Locate cells.
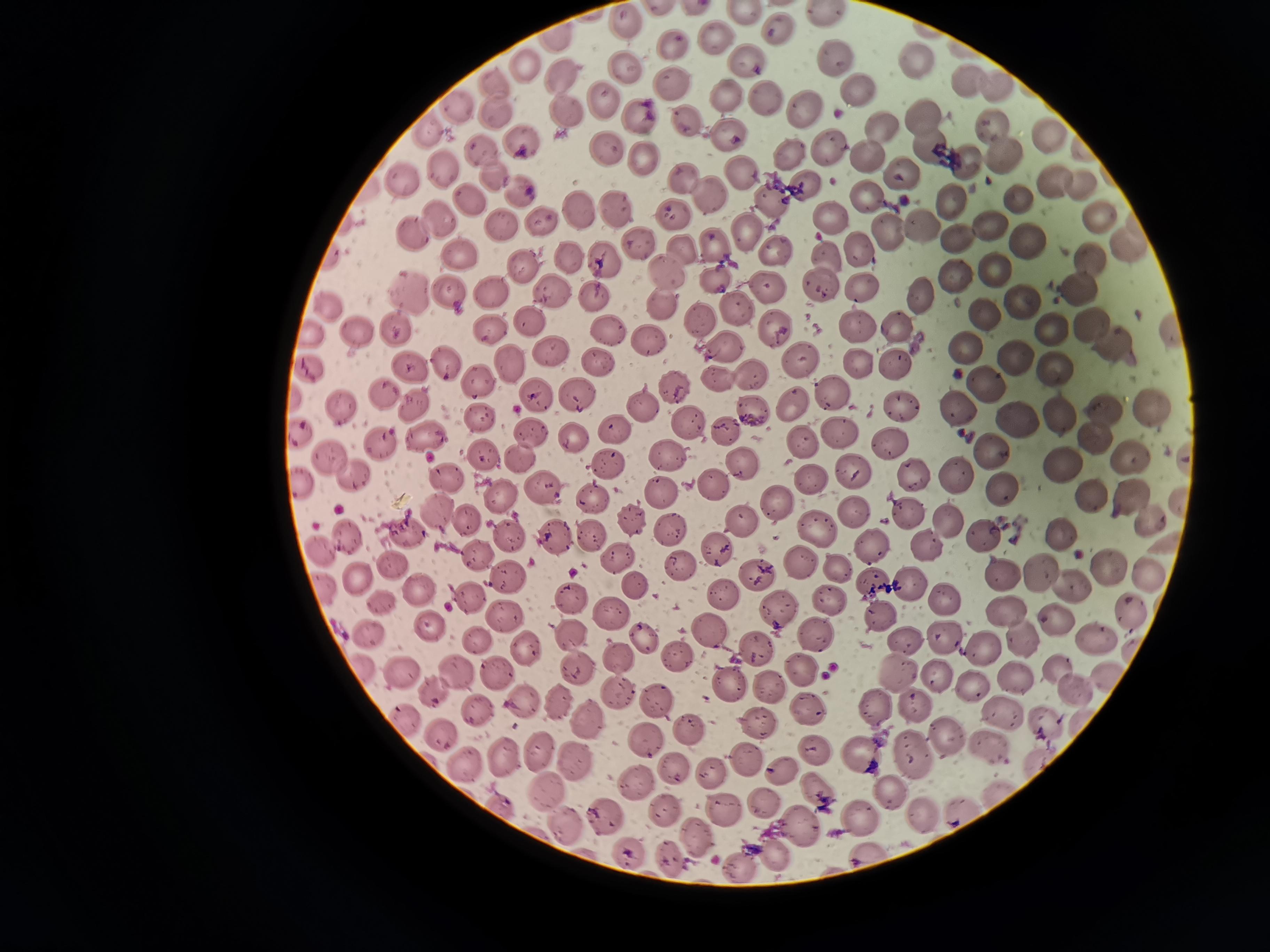

Approximate centers as [x, y] in pixels.
Cells: [625, 22], [779, 30], [715, 38], [673, 47], [835, 59], [746, 60], [910, 62], [524, 65], [625, 69], [559, 76], [964, 80], [496, 85], [671, 86], [860, 88], [996, 89], [724, 95], [603, 98], [767, 98], [803, 106], [457, 109], [498, 112], [563, 114], [636, 115], [924, 115], [993, 124], [879, 126], [728, 134], [1050, 137], [928, 141], [522, 142], [829, 146], [607, 148], [790, 150], [481, 152], [644, 155], [1004, 156], [868, 158], [967, 159], [443, 167], [739, 172], [900, 173], [683, 176], [495, 177], [403, 180], [801, 181], [1054, 182], [1080, 183], [521, 190], [709, 194], [866, 197], [470, 200], [768, 200], [1017, 201], [953, 202], [617, 209], [577, 210], [1098, 214], [673, 215], [831, 216], [541, 219], [437, 220], [504, 226], [991, 226], [918, 228], [745, 229], [956, 232], [889, 233], [412, 234], [1123, 240], [1029, 242], [639, 243], [860, 248], [683, 250], [774, 252], [459, 253], [569, 255], [604, 259], [1085, 259], [525, 265], [996, 270], [663, 272], [717, 279], [956, 281], [767, 285], [820, 285], [866, 287], [1080, 288], [408, 291], [551, 291], [922, 291], [449, 294], [594, 296], [1023, 301], [658, 303], [325, 306], [737, 308], [982, 312], [700, 316], [528, 321], [857, 326], [1095, 326], [394, 327], [1051, 328], [608, 329], [776, 329], [898, 329], [490, 330], [359, 332], [650, 340], [724, 347], [967, 348], [1113, 349], [551, 352], [1015, 354], [800, 360], [442, 361], [598, 361], [509, 363], [896, 364], [407, 365], [857, 365], [1055, 368], [717, 378], [479, 381], [987, 385], [673, 387], [834, 391], [386, 393], [533, 396], [577, 396], [414, 403], [792, 403], [903, 403], [640, 405], [956, 407], [752, 408], [1149, 410], [342, 411], [1103, 412], [1055, 416], [481, 418], [1018, 421], [687, 422], [723, 431], [836, 431], [532, 433], [426, 437], [572, 438], [891, 440], [802, 442], [1095, 442], [382, 444], [993, 451], [484, 454], [333, 456], [522, 456], [667, 456], [1126, 457], [740, 462], [607, 464], [1062, 467], [854, 470], [958, 474], [912, 475], [349, 479], [447, 479], [811, 482], [714, 483], [1000, 486], [543, 490], [663, 491], [501, 496], [1089, 496], [592, 497], [1130, 497], [777, 503], [851, 509], [440, 510], [909, 511], [1147, 518], [468, 520], [633, 521], [740, 522], [947, 524], [408, 529], [668, 530], [816, 532], [589, 533], [1058, 534], [506, 536], [554, 536], [981, 536], [351, 537], [872, 542], [924, 545], [719, 548], [326, 549], [618, 557], [799, 564], [392, 565], [1105, 565], [678, 567], [836, 567], [1035, 570], [1000, 571], [1148, 574], [755, 575], [361, 577], [508, 578], [635, 584], [912, 585], [1067, 585], [871, 586], [422, 589], [720, 594], [946, 597], [469, 598], [574, 599], [829, 601], [380, 602], [1010, 609], [1126, 609], [779, 610], [611, 614], [505, 615], [1057, 617], [878, 618], [427, 624], [367, 628], [568, 633], [711, 633], [818, 634], [644, 637], [902, 637], [948, 637], [479, 639], [1095, 639], [1025, 640], [527, 647], [756, 648], [985, 650], [619, 656], [677, 657], [578, 666], [403, 668], [1060, 668], [896, 670], [460, 671], [497, 671], [801, 672], [936, 673], [1017, 676], [728, 684], [768, 685], [433, 687], [1074, 688], [976, 690], [618, 691], [522, 699], [657, 702], [560, 703], [876, 703], [916, 703], [475, 707], [810, 709], [998, 711], [588, 718], [759, 723], [1040, 726], [690, 727], [442, 733], [953, 735], [645, 741], [990, 746], [537, 751], [816, 751], [911, 752], [860, 753], [503, 757], [746, 758], [575, 761], [467, 763], [778, 768], [711, 772], [637, 781], [545, 786], [820, 787], [889, 787], [764, 803], [668, 808], [724, 808], [917, 814], [603, 815], [860, 816], [563, 824], [798, 824], [695, 835], [627, 853], [776, 854], [739, 862].

{
  "stain": "Giemsa",
  "field_of_view": "single",
  "preparation": "thin smear",
  "capture": "smartphone camera at the microscope eyepiece",
  "image_size": "1270×952 pixels"
}